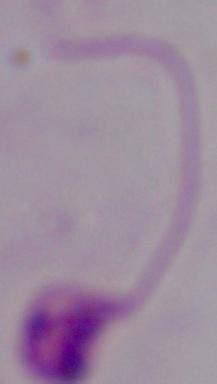

A Leishmania parasite is shown. Photomicrograph. 1000x magnification.